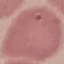

Result: no malaria parasites seen. Thin smear of blood. Cell patch, automatically extracted from a larger field of view and resized to 64 × 64 pixels. Acquired by smartphone through the microscope eyepiece. Giemsa-stained preparation.